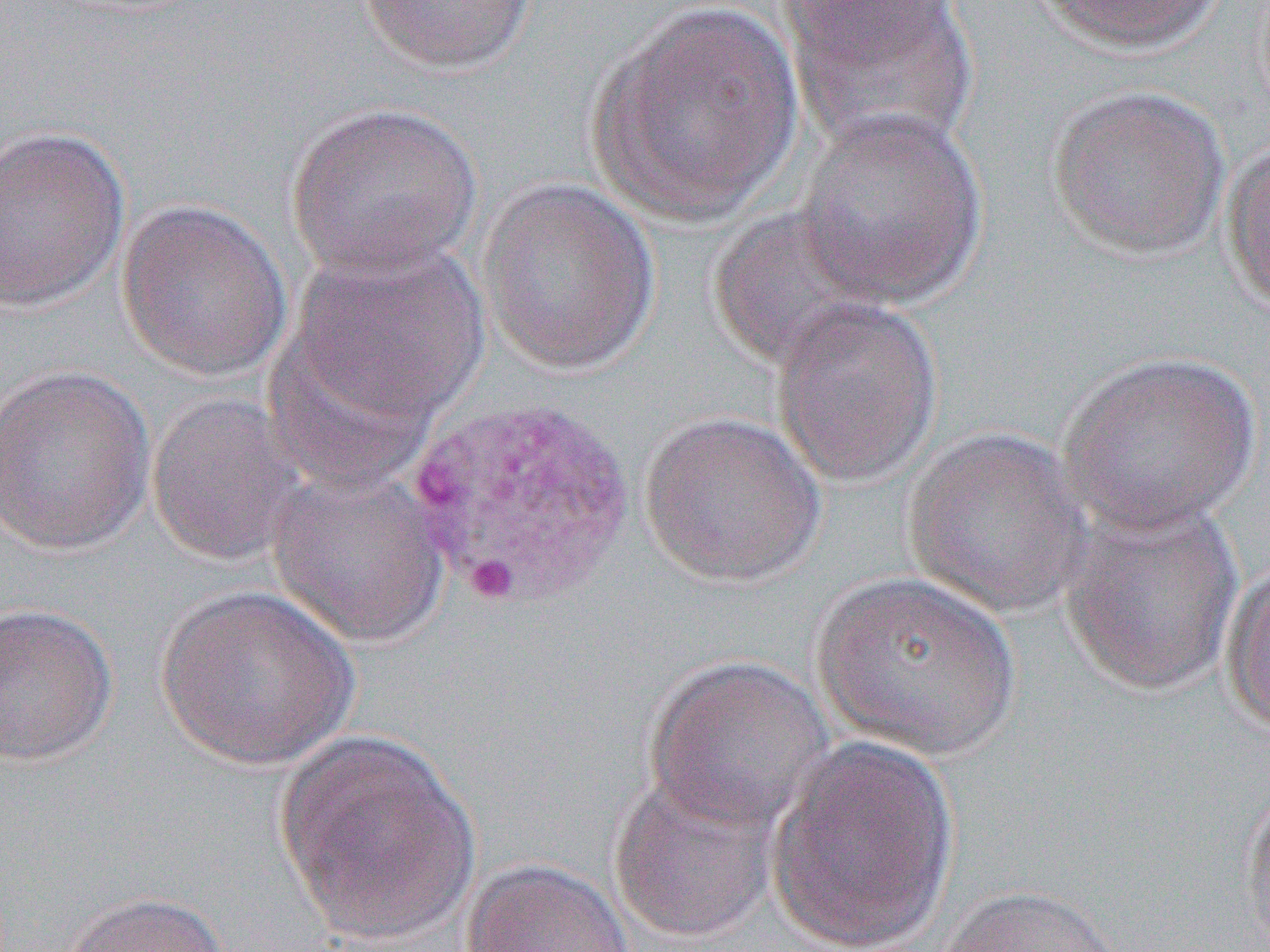

Summary:
  - Coordinate format: approximate bounding boxes as named x1/y1/x2/y2 corners in pixels
  - Uninfected red blood cell locations: (x1=356, y1=0, x2=539, y2=76), (x1=772, y1=0, x2=968, y2=65), (x1=1025, y1=0, x2=1232, y2=55), (x1=592, y1=3, x2=805, y2=224), (x1=778, y1=3, x2=980, y2=155), (x1=1046, y1=84, x2=1230, y2=260), (x1=285, y1=102, x2=484, y2=280), (x1=794, y1=107, x2=989, y2=308), (x1=0, y1=126, x2=131, y2=311), (x1=1221, y1=136, x2=1270, y2=316), (x1=477, y1=179, x2=661, y2=375), (x1=116, y1=199, x2=293, y2=382), (x1=708, y1=205, x2=891, y2=373), (x1=288, y1=241, x2=491, y2=428), (x1=771, y1=299, x2=943, y2=487), (x1=1058, y1=350, x2=1260, y2=537), (x1=0, y1=362, x2=156, y2=556), (x1=146, y1=393, x2=308, y2=567), (x1=637, y1=410, x2=827, y2=588), (x1=903, y1=427, x2=1092, y2=617), (x1=265, y1=465, x2=450, y2=647), (x1=1058, y1=496, x2=1244, y2=699), (x1=1223, y1=560, x2=1270, y2=739), (x1=811, y1=569, x2=1022, y2=760), (x1=156, y1=584, x2=360, y2=769), (x1=0, y1=602, x2=118, y2=766), (x1=642, y1=655, x2=834, y2=835), (x1=274, y1=728, x2=481, y2=945), (x1=766, y1=735, x2=961, y2=949), (x1=607, y1=771, x2=779, y2=945), (x1=1238, y1=778, x2=1270, y2=952), (x1=461, y1=858, x2=636, y2=952), (x1=936, y1=884, x2=1129, y2=952), (x1=60, y1=890, x2=229, y2=952)
  - Slide-level diagnosis: Plasmodium vivax
  - Modality: light microscopy
  - Image size: 1270×952 pixels
  - Field of view: one of a larger specimen
  - Preparation: thin blood film
  - Magnification: 1000x